Give the extent of all Plasmodium malariae-infected red blood cells.
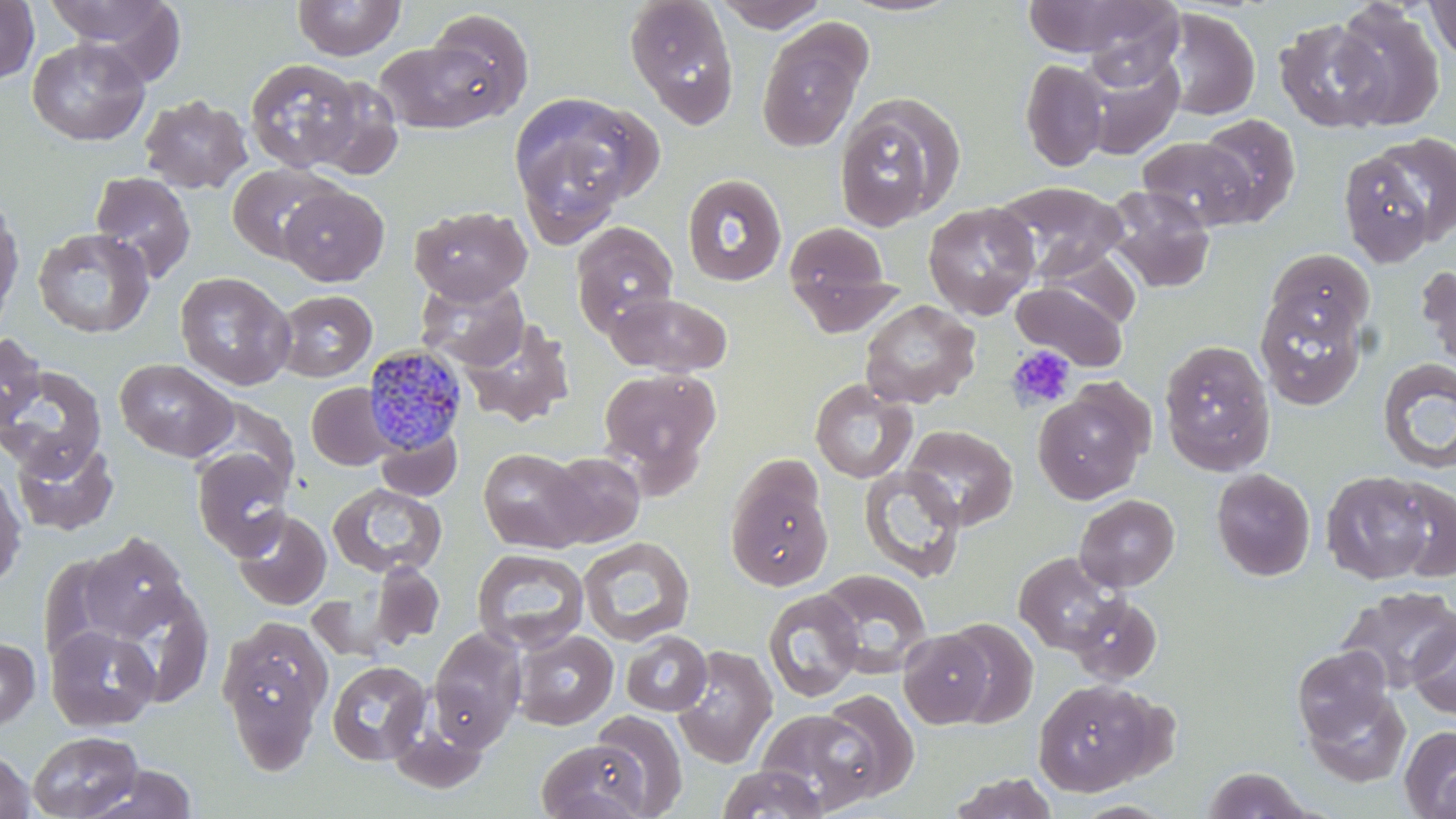

Approximate bounding boxes as named x1/y1/x2/y2 corners in pixels.
Plasmodium malariae-infected red blood cells: (x1=362, y1=344, x2=470, y2=455).

Summary:
  - Uninfected red blood cell locations: (x1=0, y1=0, x2=39, y2=84), (x1=42, y1=0, x2=185, y2=72), (x1=292, y1=0, x2=406, y2=60), (x1=624, y1=0, x2=741, y2=129), (x1=712, y1=0, x2=831, y2=32), (x1=837, y1=0, x2=965, y2=18), (x1=1022, y1=0, x2=1154, y2=58), (x1=1077, y1=0, x2=1185, y2=88), (x1=1424, y1=1, x2=1456, y2=61), (x1=1331, y1=3, x2=1445, y2=131), (x1=1159, y1=7, x2=1260, y2=121), (x1=419, y1=9, x2=535, y2=121), (x1=756, y1=16, x2=873, y2=154), (x1=1274, y1=17, x2=1392, y2=132), (x1=374, y1=36, x2=514, y2=135), (x1=27, y1=37, x2=150, y2=146), (x1=1076, y1=49, x2=1185, y2=159), (x1=244, y1=58, x2=366, y2=173), (x1=1019, y1=59, x2=1109, y2=172), (x1=307, y1=77, x2=404, y2=179), (x1=507, y1=91, x2=655, y2=236), (x1=139, y1=94, x2=252, y2=194), (x1=833, y1=94, x2=963, y2=232), (x1=1196, y1=113, x2=1301, y2=225), (x1=1137, y1=137, x2=1258, y2=229), (x1=1338, y1=143, x2=1444, y2=266), (x1=227, y1=162, x2=342, y2=263), (x1=90, y1=171, x2=196, y2=282), (x1=681, y1=173, x2=788, y2=286), (x1=994, y1=181, x2=1129, y2=283), (x1=277, y1=185, x2=388, y2=286), (x1=1102, y1=185, x2=1217, y2=293), (x1=0, y1=194, x2=24, y2=326), (x1=922, y1=201, x2=1041, y2=319), (x1=410, y1=205, x2=533, y2=305), (x1=782, y1=220, x2=896, y2=328), (x1=570, y1=222, x2=679, y2=337), (x1=32, y1=226, x2=155, y2=338), (x1=1035, y1=247, x2=1141, y2=329), (x1=1265, y1=248, x2=1374, y2=344), (x1=1416, y1=262, x2=1456, y2=372), (x1=174, y1=271, x2=297, y2=391), (x1=415, y1=277, x2=529, y2=371), (x1=1012, y1=280, x2=1128, y2=371), (x1=1254, y1=288, x2=1368, y2=410), (x1=274, y1=289, x2=377, y2=382), (x1=604, y1=291, x2=733, y2=377), (x1=859, y1=299, x2=981, y2=409), (x1=460, y1=318, x2=574, y2=428), (x1=0, y1=332, x2=46, y2=431), (x1=1158, y1=339, x2=1276, y2=475), (x1=115, y1=358, x2=238, y2=462), (x1=1376, y1=358, x2=1456, y2=476), (x1=1, y1=364, x2=107, y2=478), (x1=597, y1=367, x2=722, y2=489), (x1=810, y1=380, x2=917, y2=483), (x1=307, y1=383, x2=396, y2=470), (x1=1032, y1=384, x2=1152, y2=505), (x1=902, y1=424, x2=1018, y2=530), (x1=375, y1=428, x2=462, y2=502), (x1=11, y1=438, x2=119, y2=536), (x1=192, y1=446, x2=294, y2=559), (x1=478, y1=448, x2=589, y2=553), (x1=544, y1=452, x2=645, y2=547), (x1=725, y1=465, x2=834, y2=592), (x1=0, y1=466, x2=27, y2=590), (x1=858, y1=466, x2=966, y2=582), (x1=1210, y1=467, x2=1315, y2=581), (x1=1321, y1=470, x2=1437, y2=584), (x1=1385, y1=477, x2=1456, y2=580), (x1=328, y1=482, x2=447, y2=578), (x1=1074, y1=494, x2=1179, y2=592), (x1=231, y1=508, x2=331, y2=611), (x1=80, y1=532, x2=192, y2=642), (x1=578, y1=537, x2=695, y2=647), (x1=472, y1=548, x2=590, y2=654), (x1=1014, y1=552, x2=1125, y2=655), (x1=367, y1=562, x2=444, y2=651), (x1=816, y1=569, x2=933, y2=677), (x1=102, y1=579, x2=215, y2=708), (x1=1338, y1=586, x2=1456, y2=693), (x1=763, y1=589, x2=863, y2=702), (x1=1068, y1=594, x2=1163, y2=685), (x1=218, y1=616, x2=333, y2=768), (x1=1408, y1=616, x2=1456, y2=719), (x1=942, y1=618, x2=1038, y2=728), (x1=45, y1=625, x2=162, y2=732), (x1=428, y1=627, x2=528, y2=751), (x1=898, y1=629, x2=996, y2=728), (x1=513, y1=630, x2=618, y2=730), (x1=620, y1=631, x2=712, y2=716), (x1=0, y1=636, x2=40, y2=731), (x1=672, y1=645, x2=778, y2=768), (x1=1291, y1=645, x2=1394, y2=744), (x1=326, y1=660, x2=431, y2=766), (x1=1032, y1=679, x2=1160, y2=796), (x1=1301, y1=688, x2=1411, y2=787), (x1=814, y1=689, x2=920, y2=803), (x1=757, y1=707, x2=881, y2=813), (x1=588, y1=710, x2=689, y2=816), (x1=388, y1=715, x2=490, y2=794), (x1=1400, y1=725, x2=1456, y2=818), (x1=27, y1=730, x2=144, y2=818), (x1=535, y1=738, x2=654, y2=819), (x1=0, y1=748, x2=36, y2=819), (x1=85, y1=764, x2=199, y2=818), (x1=716, y1=764, x2=828, y2=819), (x1=1201, y1=766, x2=1316, y2=818), (x1=947, y1=772, x2=1059, y2=819)
  - Platelet locations: (x1=1007, y1=345, x2=1076, y2=411)
  - Slide-level diagnosis: Plasmodium malariae
  - Image size: 1456×819 pixels
  - Field of view: one of a larger specimen
  - Stain: May-Grünwald-Giemsa
  - Magnification: 1000x
  - Preparation: thin blood film
  - Modality: optical microscopy